Comment on the morphology of the red blood cells.
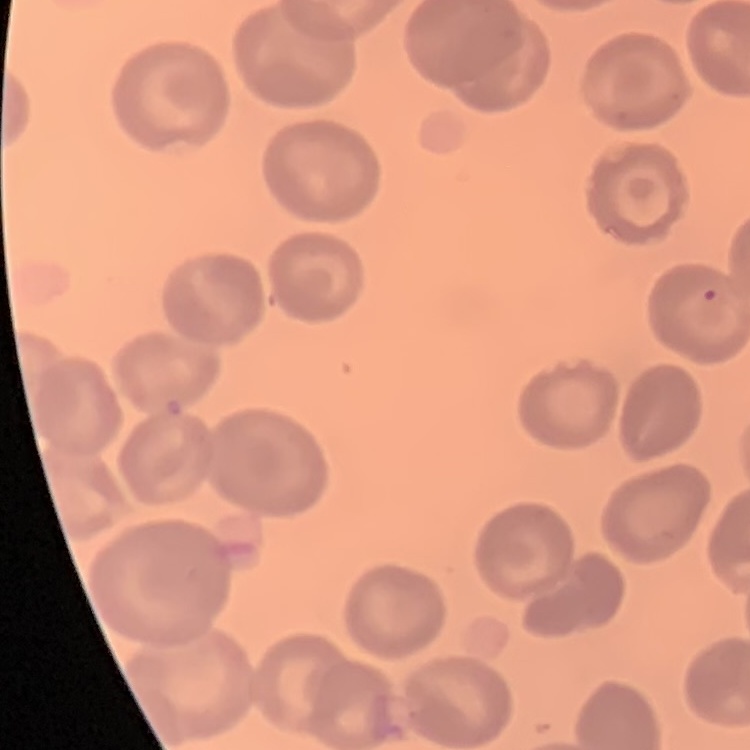

No rouleaux formation.

Square crop of a larger photomicrograph. Thin peripheral smear. Field's or Giemsa stain.